Outline each blood parasite and name the species.
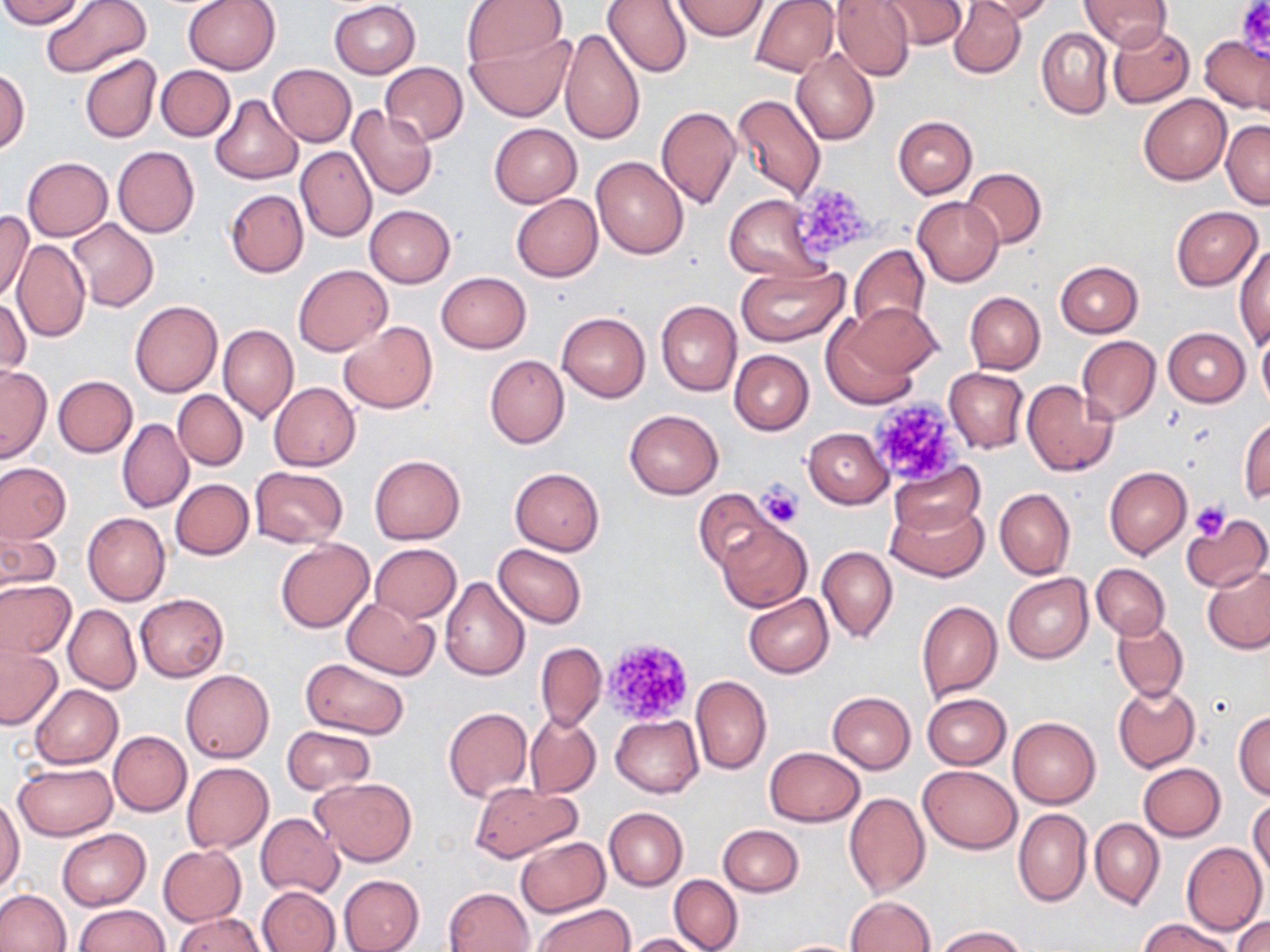

No blood parasites observed.

{
  "slide_level_diagnosis": "no evidence of blood parasites",
  "uninfected_red_blood_cell_locations": "approximate bounding boxes as [x1, y1, x2, y2] in pixels: [0, 0, 87, 27], [41, 0, 152, 77], [182, 0, 281, 75], [461, 0, 567, 69], [602, 0, 692, 77], [751, 0, 838, 76], [831, 0, 916, 81], [877, 0, 967, 50], [949, 0, 1027, 78], [968, 0, 1055, 23], [1078, 0, 1172, 51], [329, 1, 421, 79], [672, 1, 768, 40], [1107, 23, 1193, 107], [559, 26, 646, 146], [1037, 27, 1112, 119], [467, 32, 576, 123], [1200, 35, 1269, 113], [791, 49, 879, 146], [80, 54, 162, 145], [380, 62, 468, 145], [267, 64, 356, 147], [156, 65, 234, 141], [0, 68, 30, 155], [731, 93, 826, 201], [1138, 94, 1231, 185], [211, 96, 302, 184], [347, 106, 438, 199], [656, 106, 742, 209], [893, 116, 977, 198], [1221, 119, 1269, 208], [489, 122, 582, 208], [113, 147, 199, 239], [296, 147, 376, 242], [591, 156, 688, 261], [22, 157, 112, 241], [962, 168, 1046, 249], [225, 189, 309, 278], [725, 193, 824, 279], [512, 194, 602, 281], [913, 198, 1003, 286], [364, 206, 455, 288], [1170, 206, 1263, 290], [1, 212, 33, 303], [68, 218, 159, 311], [12, 239, 91, 343], [849, 244, 931, 334], [1235, 244, 1269, 348], [1056, 261, 1143, 337], [293, 264, 393, 356], [735, 265, 848, 346], [436, 271, 531, 353], [956, 291, 1036, 453], [965, 291, 1045, 374], [1, 295, 30, 383], [131, 300, 223, 397], [654, 300, 742, 396], [839, 303, 939, 388], [556, 311, 650, 401], [338, 321, 438, 414], [218, 325, 298, 424], [1163, 328, 1249, 406], [1257, 332, 1270, 411], [1076, 336, 1161, 423], [729, 349, 814, 435], [485, 354, 569, 449], [0, 365, 51, 462], [944, 367, 1029, 453], [53, 375, 138, 458], [1022, 379, 1119, 476], [269, 382, 360, 470], [173, 390, 248, 471], [624, 409, 724, 499], [1239, 416, 1269, 503], [117, 418, 194, 513], [803, 427, 893, 508], [369, 455, 465, 544], [889, 460, 983, 536], [0, 462, 71, 543], [1104, 466, 1191, 559], [250, 467, 348, 547], [510, 468, 604, 554], [171, 479, 254, 560], [694, 488, 783, 574], [995, 489, 1075, 579], [887, 498, 988, 582], [82, 512, 170, 606], [1185, 515, 1270, 592], [716, 523, 811, 611], [1, 530, 61, 591], [275, 538, 374, 632], [494, 543, 586, 627], [371, 544, 461, 622], [818, 545, 897, 643], [1093, 564, 1170, 639], [1203, 565, 1270, 654], [1003, 574, 1093, 662], [440, 575, 530, 681], [0, 580, 76, 659], [135, 593, 229, 683], [744, 594, 833, 677], [340, 598, 440, 679], [916, 601, 1002, 702], [63, 603, 141, 694], [1112, 619, 1188, 701], [536, 642, 606, 731], [0, 645, 64, 729], [300, 658, 410, 739], [181, 669, 273, 763], [690, 675, 772, 775], [1113, 683, 1201, 772], [29, 684, 122, 769], [827, 691, 916, 772], [923, 692, 1011, 768], [444, 707, 531, 801], [1234, 710, 1270, 799], [526, 712, 601, 798], [610, 715, 702, 797], [1008, 716, 1100, 808], [282, 725, 375, 793], [108, 731, 192, 816], [763, 747, 866, 827], [182, 761, 273, 852], [14, 762, 116, 840], [1137, 762, 1226, 841], [919, 765, 1021, 853], [311, 778, 417, 865], [469, 782, 583, 862], [842, 791, 929, 897], [0, 795, 25, 893], [1248, 797, 1269, 887], [604, 808, 687, 890], [1013, 808, 1092, 906], [256, 814, 344, 897], [1091, 817, 1163, 909], [718, 825, 803, 897], [56, 829, 151, 909], [515, 837, 609, 918], [1182, 841, 1267, 934], [158, 845, 246, 926], [669, 874, 743, 952], [338, 875, 424, 952], [258, 887, 341, 952], [444, 887, 534, 952], [0, 889, 71, 952], [846, 895, 935, 951], [74, 904, 170, 951], [534, 904, 633, 952], [175, 913, 268, 952], [1234, 916, 1270, 952], [1136, 917, 1237, 952], [933, 925, 1027, 951], [625, 933, 707, 952], [772, 939, 866, 951]",
  "platelet_locations": "approximate bounding boxes as [x1, y1, x2, y2] in pixels: [1235, 0, 1269, 58], [789, 182, 877, 262], [870, 390, 962, 490], [757, 480, 804, 529], [1188, 501, 1230, 542], [599, 637, 695, 726]",
  "magnification": "1000x",
  "image_size": "1270×952 pixels",
  "field_of_view": "one of a larger specimen",
  "stain": "May-Grünwald-Giemsa",
  "preparation": "thin blood film",
  "modality": "optical microscopy"
}